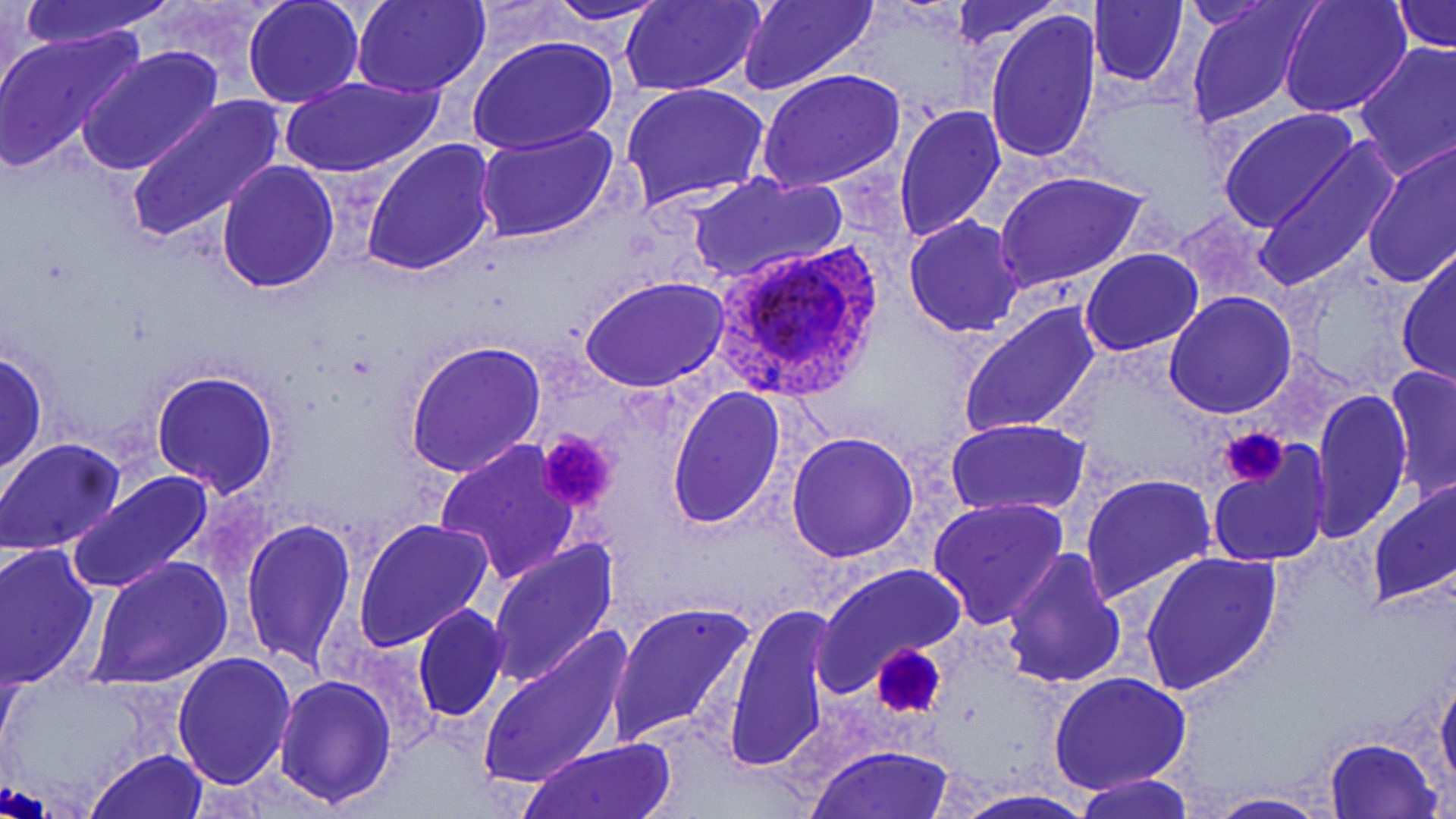
Summary:
  - Coordinate format: approximate bounding boxes as (x1, y1, x2, y2) in pixels
  - Uninfected red blood cell locations: (17, 0, 175, 49), (242, 0, 363, 108), (352, 0, 490, 97), (543, 0, 675, 25), (620, 0, 765, 94), (737, 0, 881, 96), (948, 0, 1060, 48), (1090, 0, 1188, 87), (1278, 0, 1410, 119), (1184, 1, 1319, 127), (1394, 1, 1453, 51), (986, 11, 1100, 165), (0, 24, 145, 174), (468, 36, 619, 156), (1352, 40, 1456, 183), (77, 45, 227, 178), (756, 68, 906, 194), (278, 74, 447, 179), (621, 83, 771, 211), (126, 95, 287, 244), (894, 103, 1006, 243), (1218, 107, 1357, 232), (474, 123, 620, 244), (360, 138, 499, 276), (1253, 139, 1401, 293), (1360, 139, 1456, 289), (216, 161, 339, 293), (995, 171, 1148, 293), (688, 173, 843, 282), (904, 216, 1026, 336), (1397, 247, 1456, 389), (1080, 249, 1202, 357), (580, 276, 729, 392), (1164, 293, 1297, 418), (959, 303, 1101, 438), (403, 341, 545, 477), (0, 350, 48, 475), (1385, 366, 1456, 499), (151, 369, 280, 497), (664, 383, 785, 529), (1310, 388, 1413, 543), (946, 418, 1091, 518), (786, 431, 918, 559), (0, 438, 126, 556), (436, 439, 582, 585), (1206, 443, 1330, 568), (67, 471, 215, 595), (1079, 473, 1217, 604), (1366, 475, 1456, 607), (928, 497, 1069, 629), (353, 517, 496, 651), (242, 518, 356, 669), (489, 538, 621, 691), (0, 542, 101, 690), (1003, 547, 1127, 689), (1137, 550, 1282, 696), (89, 557, 233, 687), (813, 563, 966, 695), (606, 600, 755, 749), (412, 602, 509, 723), (724, 602, 835, 770), (476, 626, 632, 791), (172, 652, 297, 790), (1436, 669, 1456, 799), (1048, 671, 1192, 793), (275, 676, 397, 808), (1323, 736, 1444, 819), (520, 740, 678, 818), (809, 743, 956, 818), (88, 749, 208, 819), (1078, 774, 1194, 819), (951, 789, 1100, 819), (1203, 792, 1330, 819)
  - Platelet locations: (1221, 425, 1289, 488), (536, 430, 619, 515), (871, 644, 948, 720)
  - Plasmodium ovale-infected red blood cell locations: (707, 242, 887, 406)
  - Slide-level diagnosis: Plasmodium ovale
  - Magnification: 1000x
  - Stain: May-Grünwald-Giemsa
  - Image size: 1456×819 pixels
  - Field of view: one of a larger specimen
  - Preparation: thin blood smear
  - Modality: light microscopy